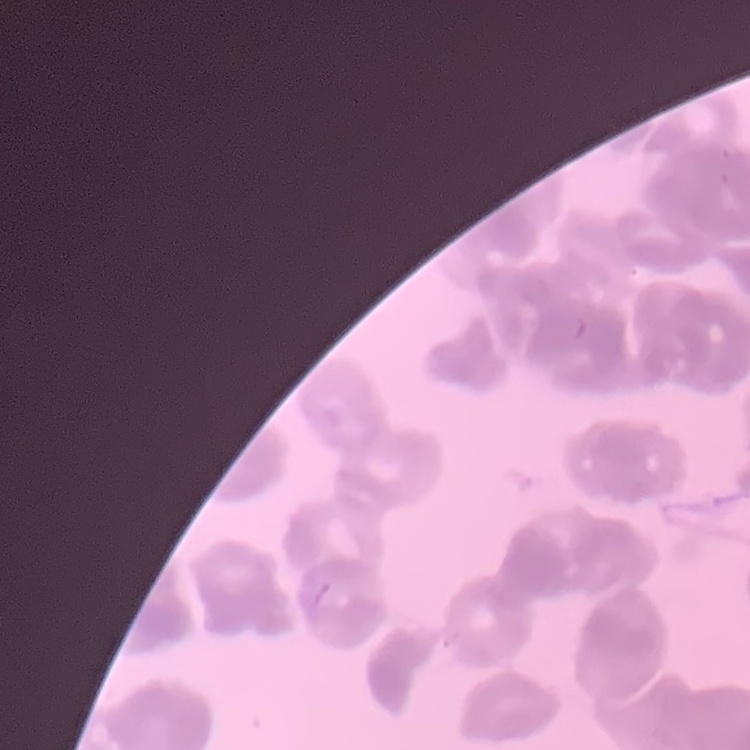

red blood cell morphology = rouleaux formation
image type = one tile cut from a larger photomicrograph
preparation = thin blood film
stain = Field's or Giemsa